Classify this cell by malaria status.
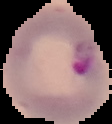

It is parasitized.

Segmented cell region on a black background. Image is 112×124 pixels. From a thin blood smear.